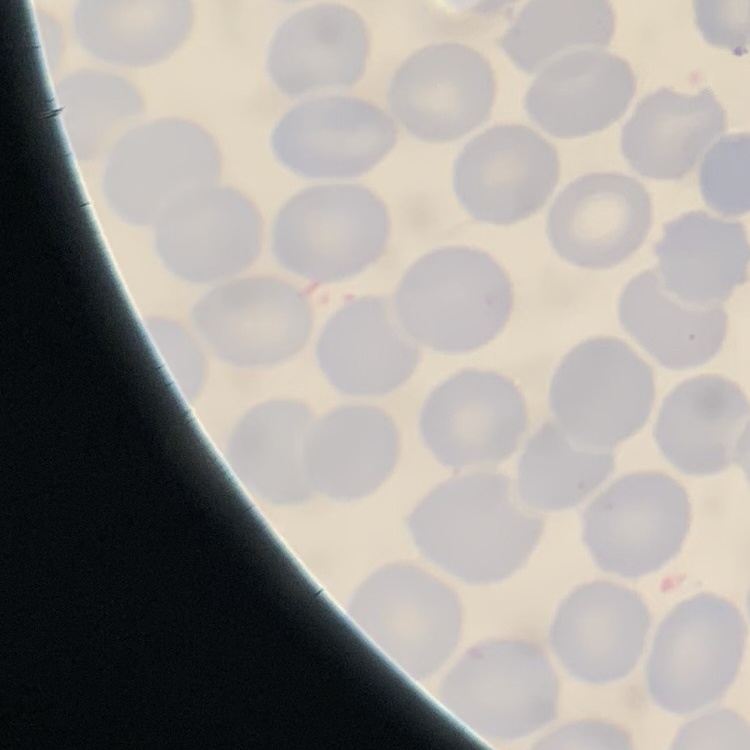

{
  "red_blood_cell_morphology": "no rouleaux formation",
  "image_type": "one tile cut from a larger photomicrograph",
  "stain": "Field's or Giemsa",
  "preparation": "thin blood smear"
}